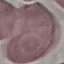

malaria status = uninfected
image type = automatically extracted cell patch, resized to 64 × 64 pixels
capture = smartphone camera at the microscope eyepiece
stain = Giemsa
preparation = thin smear